Outline each blood parasite and name the species.
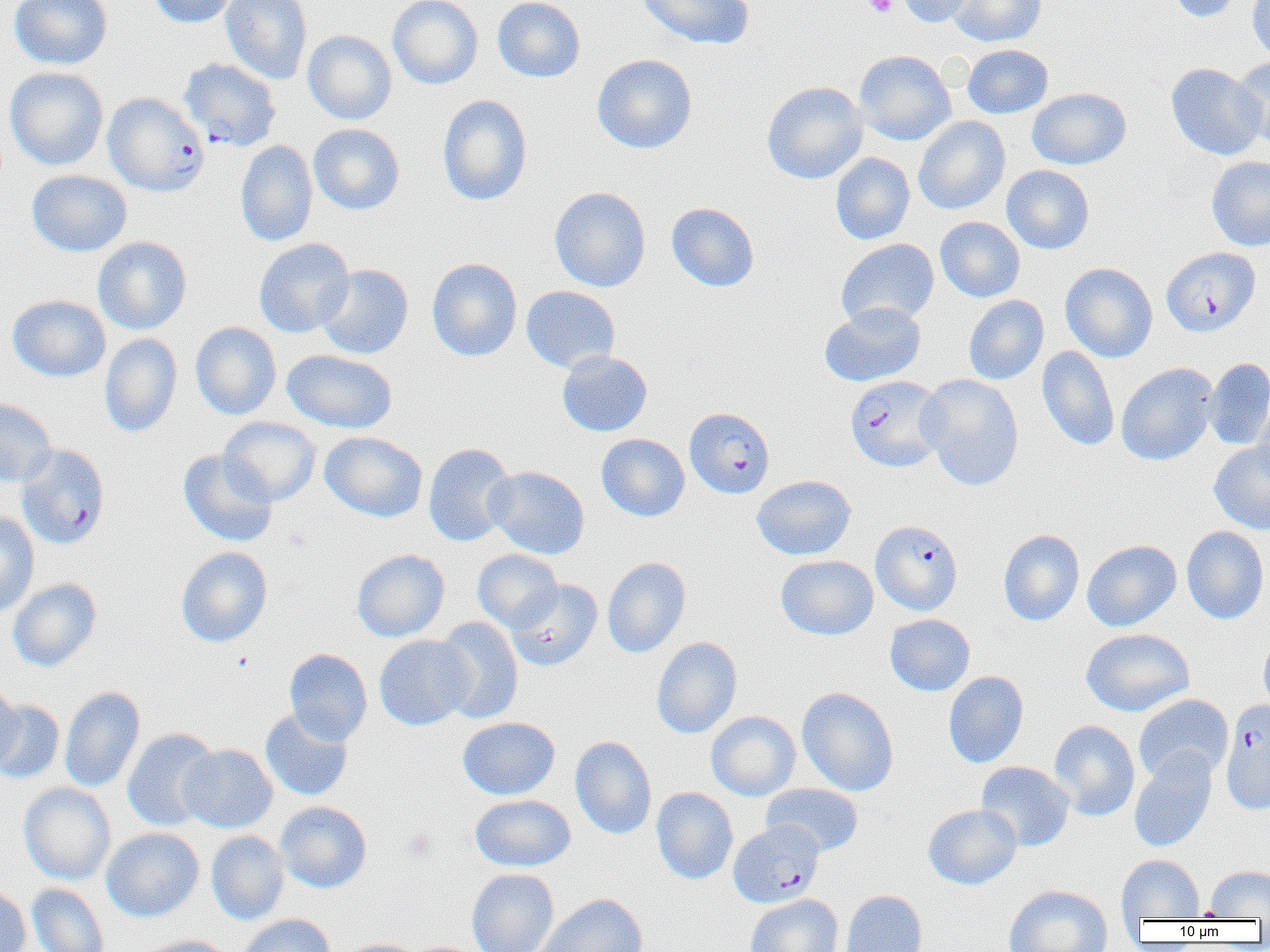

Approximate bounding boxes as [x1, y1, x2, y2] in pixels.
Plasmodium falciparum-infected red blood cells (subset): [178, 58, 282, 151], [103, 93, 209, 197], [1162, 247, 1260, 337], [845, 375, 947, 472], [684, 407, 774, 498], [871, 520, 963, 615], [1220, 699, 1270, 815], [728, 821, 824, 907].
No Plasmodium ovale, Plasmodium malariae, Plasmodium vivax, Babesia divergens, or Trypanosoma brucei observed.

Summary:
  - Platelet locations: [864, 0, 897, 17], [403, 829, 437, 860]
  - Uninfected red blood cell locations (subset): [9, 0, 112, 70], [149, 0, 241, 28], [220, 0, 312, 84], [387, 0, 483, 89], [492, 0, 586, 82], [636, 0, 755, 50], [896, 0, 980, 27], [947, 0, 1047, 47], [1165, 0, 1247, 23], [1247, 0, 1270, 63], [302, 30, 397, 125], [963, 44, 1053, 118], [854, 50, 956, 145], [592, 53, 697, 154], [1231, 56, 1270, 148], [1166, 63, 1266, 160], [4, 67, 108, 171], [762, 81, 868, 184], [1027, 88, 1131, 170], [438, 94, 533, 206], [913, 116, 1010, 214], [308, 124, 405, 215], [236, 139, 318, 247], [830, 152, 915, 245], [1207, 156, 1270, 251], [1001, 165, 1094, 254], [27, 170, 132, 257], [549, 186, 651, 292], [666, 202, 759, 292], [935, 216, 1025, 302], [92, 236, 192, 334], [254, 238, 355, 338], [836, 238, 939, 327], [426, 258, 522, 361], [1060, 262, 1158, 362], [315, 264, 414, 360], [521, 285, 620, 373], [7, 295, 111, 382], [963, 295, 1049, 385], [820, 302, 926, 387], [190, 321, 281, 420], [99, 333, 182, 438], [1037, 346, 1120, 451], [282, 349, 397, 433], [557, 350, 652, 437], [1205, 357, 1270, 450], [1116, 362, 1218, 466], [917, 374, 1024, 491], [0, 398, 58, 487], [1253, 398, 1270, 492], [219, 417, 321, 506], [320, 431, 427, 522], [596, 433, 690, 521], [1209, 442, 1270, 535], [423, 443, 517, 546], [178, 449, 278, 547], [485, 465, 590, 559], [752, 475, 857, 560], [0, 510, 40, 617], [1181, 526, 1269, 624], [998, 529, 1084, 626], [1082, 540, 1181, 631], [176, 546, 273, 647], [352, 549, 450, 642], [472, 549, 563, 632], [776, 555, 878, 640], [602, 556, 691, 658], [7, 578, 102, 672], [506, 579, 603, 671], [885, 614, 975, 695], [433, 617, 524, 723], [1080, 628, 1195, 717], [1258, 628, 1270, 719], [374, 635, 475, 730], [652, 637, 742, 739], [284, 648, 373, 745], [943, 671, 1029, 768], [0, 682, 21, 770], [59, 686, 146, 793], [797, 687, 899, 796], [1134, 694, 1234, 784], [0, 700, 65, 784], [259, 708, 354, 801], [706, 710, 801, 801], [457, 717, 560, 800], [1048, 720, 1140, 821], [122, 728, 220, 831], [570, 736, 657, 839], [177, 744, 278, 832], [1129, 750, 1217, 852], [976, 761, 1074, 851], [19, 782, 116, 885], [762, 783, 864, 857], [651, 787, 738, 884], [470, 794, 576, 872], [275, 801, 372, 893], [923, 803, 1022, 889], [101, 827, 204, 922], [206, 830, 289, 925], [1116, 855, 1204, 920], [1205, 864, 1270, 919], [467, 868, 560, 952], [27, 883, 110, 952], [0, 884, 31, 952], [1003, 884, 1113, 952], [839, 890, 928, 952], [534, 893, 648, 952], [745, 894, 843, 952], [238, 914, 335, 952], [131, 935, 236, 952], [336, 938, 422, 952]
  - Slide-level diagnosis: Plasmodium falciparum
  - Preparation: thin blood film
  - Field of view: one of a larger specimen
  - Magnification: 1000x
  - Image size: 1270×952 pixels
  - Modality: optical microscopy